Locate every malaria parasite.
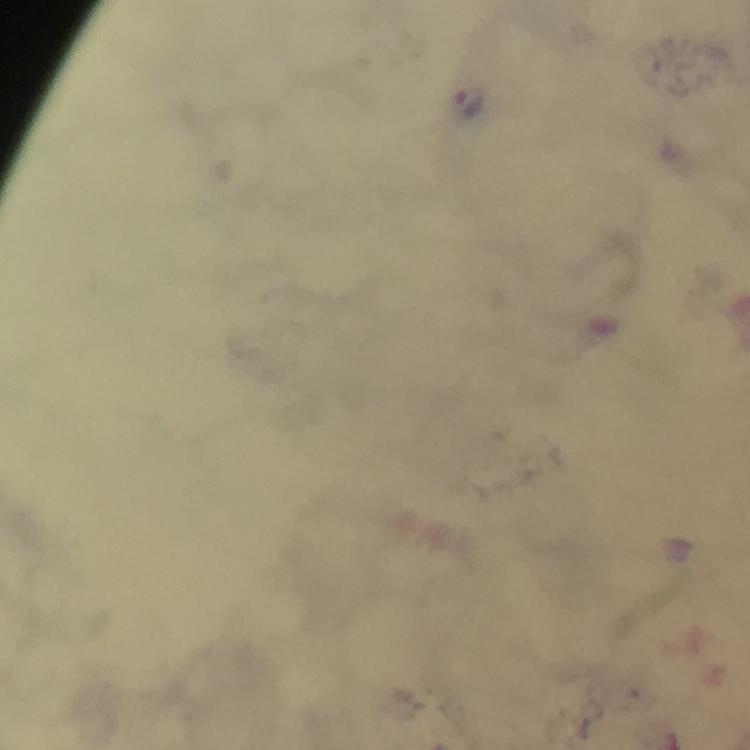

Approximate object centers, in pixels from the top-left corner.
Malaria parasites: (x=471, y=106).

cropped from = a single field of view
magnification = 100x
image size = 750×750 pixels
immersion oil = used
preparation = thick blood smear
stain = Giemsa
context = from a malaria diagnostic workup
capture = smartphone camera through the microscope